Identify the parasite.
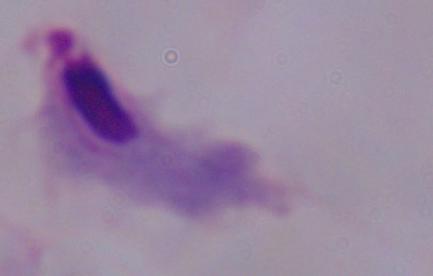
A trichomonad.

Micrograph. 1000x magnification.